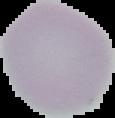

From a thin blood smear. Cell region segmented out of the field of view; the surrounding area is masked to black. Image is 115×118 pixels. Result: no malaria parasites seen.